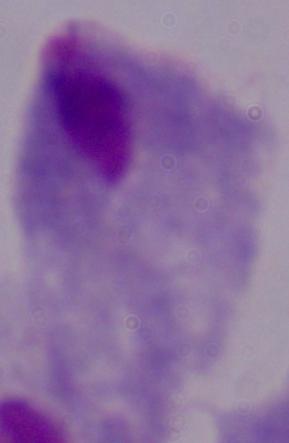 Micrograph. A trichomonad is seen. Captured at 1000x magnification.